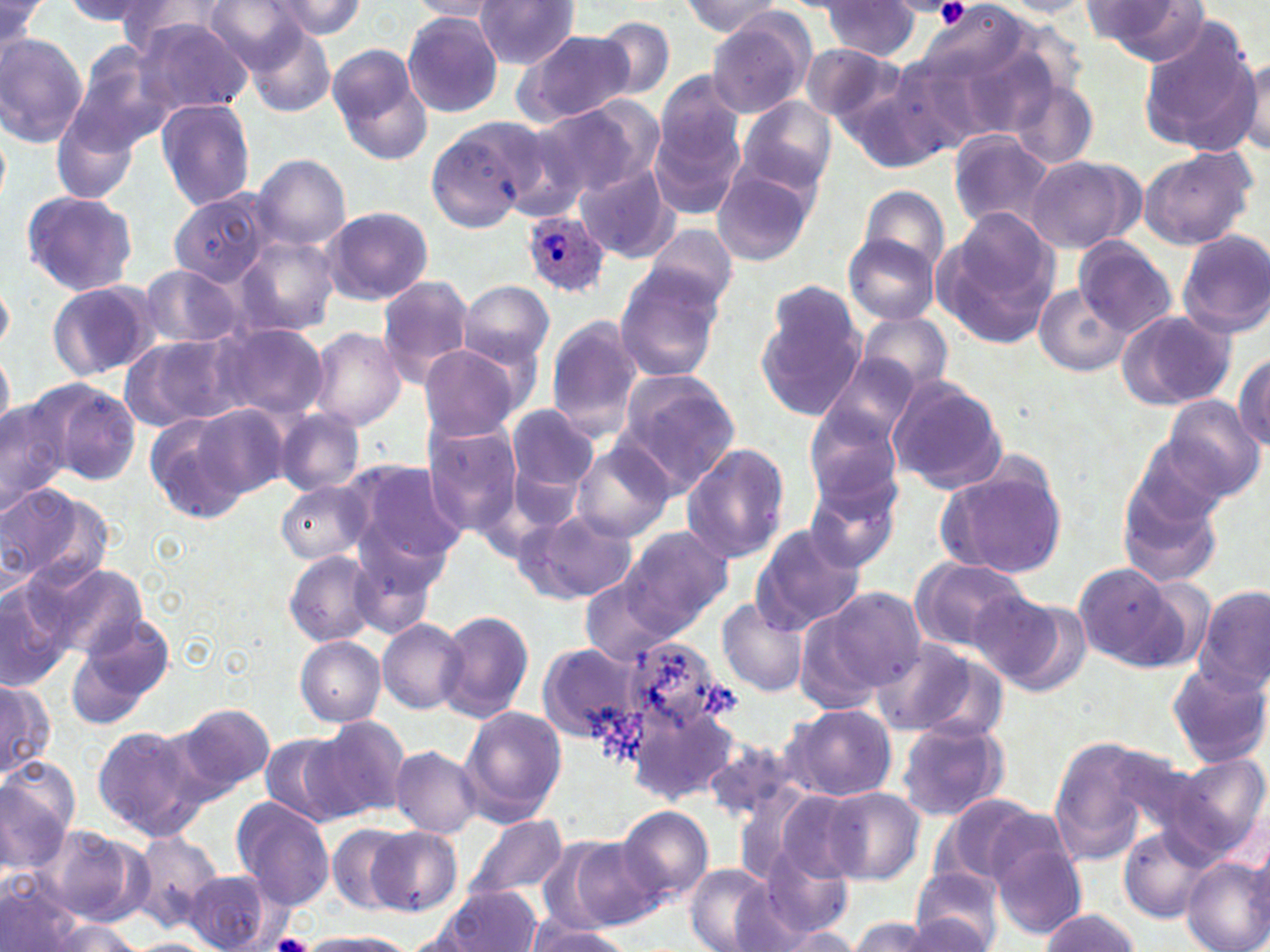
Approximate bounding boxes as (x1,y1)-(x2,y2) corner pairs in pixels. Plasmodium ovale-infected red blood cell locations: (521,208)-(610,299). Uninfected red blood cell locations: (64,0)-(171,33), (113,0)-(226,61), (201,0)-(316,73), (271,0)-(367,39), (474,0)-(580,68), (407,1)-(501,22), (680,1)-(787,39), (817,1)-(924,61), (995,1)-(1095,16), (1082,1)-(1207,64), (0,2)-(45,49), (401,11)-(504,118), (706,12)-(815,118), (132,16)-(253,117), (593,16)-(676,98), (1133,19)-(1261,153), (244,26)-(336,115), (517,29)-(637,126), (0,33)-(88,146), (801,43)-(905,125), (327,44)-(432,165), (67,45)-(171,157), (1236,52)-(1270,157), (891,54)-(994,155), (843,60)-(967,171), (653,69)-(748,172), (1004,76)-(1100,171), (737,95)-(837,195), (155,99)-(255,210), (534,101)-(659,203), (648,111)-(744,221), (477,116)-(589,221), (424,119)-(541,233), (948,129)-(1056,231), (1138,144)-(1258,249), (252,153)-(351,251), (1023,156)-(1143,254), (710,165)-(819,266), (574,166)-(678,263), (857,186)-(948,278), (20,189)-(139,298), (162,190)-(272,325), (320,205)-(434,305), (933,209)-(1060,347), (642,224)-(739,316), (1176,229)-(1270,339), (843,233)-(941,324), (235,234)-(339,335), (1072,237)-(1178,336), (137,264)-(244,348), (613,269)-(724,382), (377,275)-(477,388), (0,277)-(15,353), (47,280)-(159,382), (458,281)-(555,372), (1034,283)-(1129,376), (756,285)-(869,421), (1114,307)-(1238,412), (855,309)-(953,396), (544,318)-(643,443), (213,322)-(327,421), (307,327)-(407,431), (121,333)-(241,432), (0,344)-(13,438), (417,344)-(525,439), (1233,352)-(1270,449), (816,353)-(921,450), (613,372)-(740,494), (886,378)-(1008,495), (42,381)-(142,488), (1161,396)-(1265,503), (0,397)-(69,517), (194,403)-(293,499), (505,403)-(601,507), (803,405)-(905,509), (274,410)-(364,496), (146,414)-(250,522), (423,421)-(524,537), (571,442)-(675,543), (680,443)-(791,564), (345,460)-(469,570), (939,465)-(1067,580), (1118,469)-(1225,591), (803,475)-(902,574), (0,481)-(103,587), (277,481)-(372,565), (517,508)-(638,604), (752,525)-(866,631), (623,526)-(734,629), (285,550)-(380,645), (907,558)-(1033,656), (1072,561)-(1184,671), (34,563)-(149,660), (579,577)-(679,665), (0,579)-(72,687), (1196,585)-(1270,693), (809,586)-(928,698), (973,590)-(1087,693), (717,599)-(808,697), (438,611)-(535,722), (68,617)-(177,728), (377,618)-(469,715), (617,632)-(730,739), (294,635)-(385,726), (873,637)-(998,739), (537,644)-(641,743), (1166,661)-(1269,768), (0,678)-(52,779), (172,702)-(275,798), (630,702)-(739,802), (783,704)-(895,801), (460,705)-(568,821), (309,715)-(412,820), (895,719)-(1011,823), (91,724)-(211,840), (258,732)-(360,827), (702,735)-(798,824), (1044,737)-(1170,862), (392,746)-(481,837), (1160,753)-(1270,862), (0,767)-(76,868), (822,788)-(924,884), (771,789)-(866,884), (935,793)-(1047,893), (231,796)-(337,911), (615,804)-(715,904), (464,814)-(570,902), (326,822)-(416,914), (35,824)-(155,928), (129,825)-(224,930), (366,826)-(461,917), (1119,827)-(1215,923), (566,838)-(666,931), (991,838)-(1087,941), (758,844)-(854,938), (1180,856)-(1270,952), (685,864)-(775,952), (908,867)-(1009,952), (184,870)-(272,952), (0,875)-(89,952), (436,886)-(545,952), (1039,909)-(1140,952), (902,915)-(991,950), (846,917)-(945,951), (40,918)-(147,951), (521,921)-(628,951), (773,928)-(862,951), (296,931)-(420,952). Platelet locations: (933,0)-(969,27), (272,933)-(314,952). Slide-level diagnosis: Plasmodium ovale. Light microscopy. Image is 1270×952 pixels. 1000x magnification. Single field of view. Thin blood film. May-Grünwald-Giemsa-stained preparation.